Locate every Plasmodium parasite and every leukocyte.
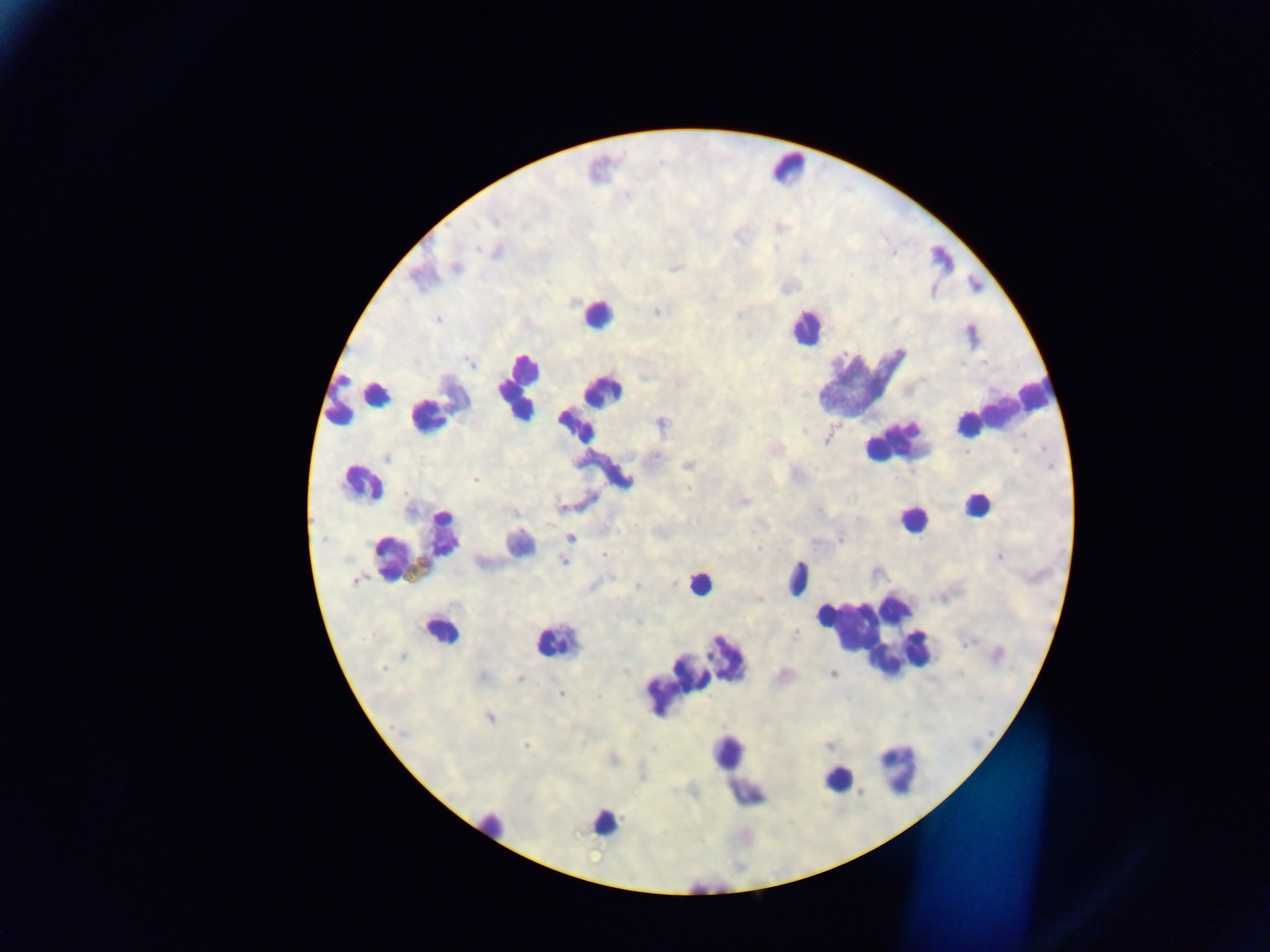

Approximate centers as {x, y} in pixels.
Plasmodium parasites: {456, 268}, {438, 319}, {387, 458}, {687, 465}, {475, 480}, {744, 500}, {562, 507}, {570, 537}, {760, 548}, {603, 555}, {998, 556}, {564, 560}, {354, 580}, {637, 586}, {481, 676}, {520, 680}, {561, 694}, {489, 717}, {525, 745}.
Leukocytes (some below the resolvable threshold): {788, 168}, {596, 314}, {805, 328}, {860, 384}, {518, 387}, {359, 394}, {455, 397}, {591, 405}, {998, 411}, {426, 418}, {892, 444}, {603, 472}, {361, 483}, {976, 505}, {911, 520}, {519, 545}, {417, 547}, {797, 578}, {698, 583}, {440, 631}, {871, 634}, {549, 644}, {695, 669}, {896, 768}, {737, 771}, {838, 779}, {603, 823}, {494, 824}.

Summary:
  - Country: Ghana
  - Image size: 1270×952 pixels
  - Field of view: single
  - Preparation: thick blood smear
  - Capture: mobile-phone photograph through a microscope